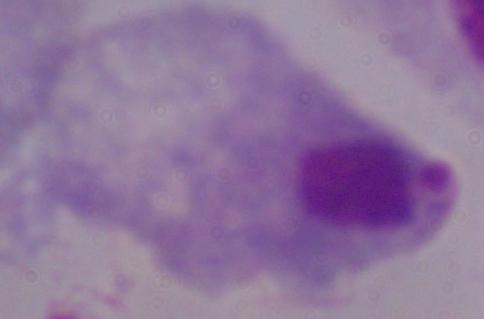

{
  "magnification": "1000x",
  "modality": "micrograph",
  "identification": "trichomonad"
}